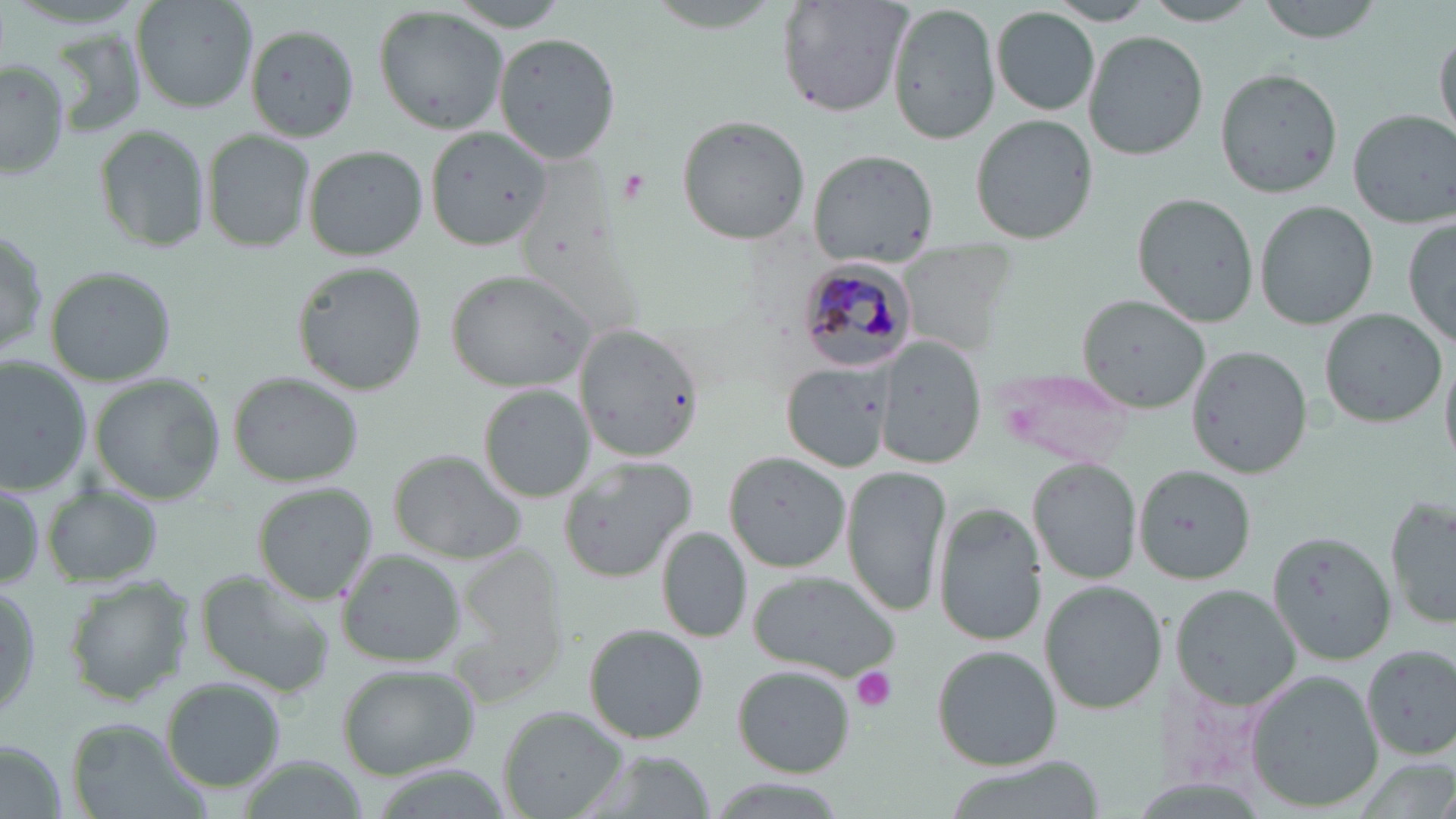

slide-level diagnosis = Plasmodium malariae
image size = 1456×819 pixels
Plasmodium malariae-infected red blood cell locations = approximate bounding boxes as (x1, y1, x2, y2) in pixels: (796, 257, 920, 370)
stain = May-Grünwald-Giemsa
modality = optical microscopy
field of view = single
uninfected red blood cell locations = approximate bounding boxes as (x1, y1, x2, y2) in pixels: (132, 0, 257, 112), (1141, 0, 1265, 25), (1257, 0, 1386, 43), (777, 1, 911, 117), (887, 1, 1000, 146), (446, 2, 575, 32), (1046, 3, 1157, 25), (373, 6, 509, 136), (991, 7, 1099, 114), (246, 24, 360, 140), (1433, 24, 1455, 143), (1083, 28, 1206, 158), (492, 31, 622, 165), (0, 59, 73, 181), (1216, 66, 1343, 197), (1348, 108, 1454, 228), (675, 114, 809, 246), (970, 114, 1097, 246), (94, 123, 211, 256), (426, 127, 549, 249), (203, 129, 313, 253), (305, 145, 428, 261), (806, 149, 938, 268), (1132, 193, 1257, 326), (1255, 201, 1377, 328), (1403, 221, 1456, 349), (1, 224, 49, 362), (291, 263, 425, 396), (45, 267, 177, 384), (449, 268, 595, 391), (1077, 295, 1212, 412), (1320, 308, 1445, 428), (576, 325, 702, 463), (875, 337, 987, 470), (1186, 347, 1314, 477), (1440, 351, 1456, 476), (1, 357, 93, 492), (781, 364, 890, 474), (990, 368, 1136, 467), (229, 372, 366, 487), (93, 377, 223, 502), (479, 388, 595, 502), (390, 451, 529, 562), (724, 452, 851, 572), (558, 456, 696, 582), (1028, 459, 1140, 584), (1136, 464, 1255, 582), (843, 465, 950, 617), (980, 470, 1113, 607), (0, 479, 46, 591), (43, 483, 163, 589), (254, 484, 376, 602), (1384, 492, 1456, 629), (933, 505, 1045, 647), (656, 528, 749, 645), (1269, 530, 1393, 664), (336, 549, 466, 667), (194, 569, 335, 696), (747, 572, 900, 682), (66, 577, 191, 704), (1040, 579, 1167, 713), (0, 584, 39, 729), (1173, 585, 1301, 707), (586, 625, 709, 744), (1360, 645, 1456, 760), (931, 646, 1058, 770), (338, 665, 480, 780), (735, 666, 854, 777), (1246, 671, 1383, 811), (162, 678, 285, 791), (499, 708, 623, 819), (68, 719, 204, 819), (2, 742, 68, 819), (577, 747, 714, 819)
preparation = thin blood film
platelet locations = approximate bounding boxes as (x1, y1, x2, y2) in pixels: (850, 666, 898, 713)
magnification = 1000x